Identify the parasite.
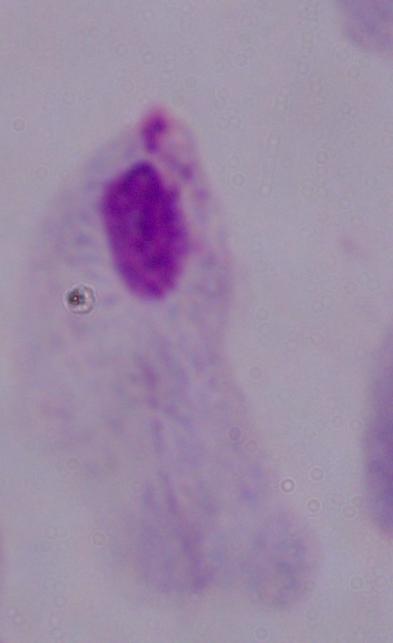

A trichomonad.

Summary:
  - Modality: photomicrograph
  - Magnification: 1000x